Describe the morphology of the erythrocytes.
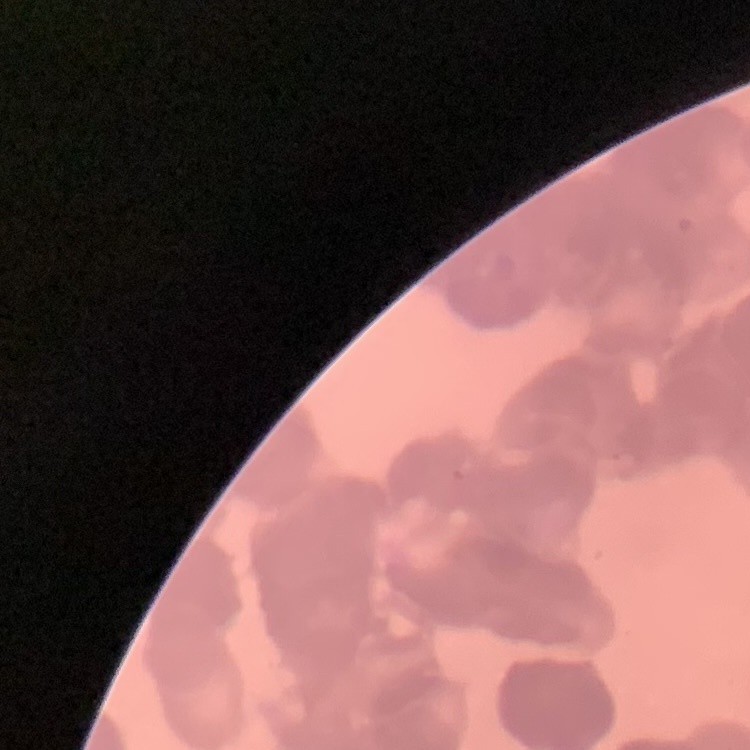

Rouleaux formation.

Square crop of a larger photomicrograph. Field's or Giemsa stain. Thin blood smear.